Describe the morphology of the red blood cells.
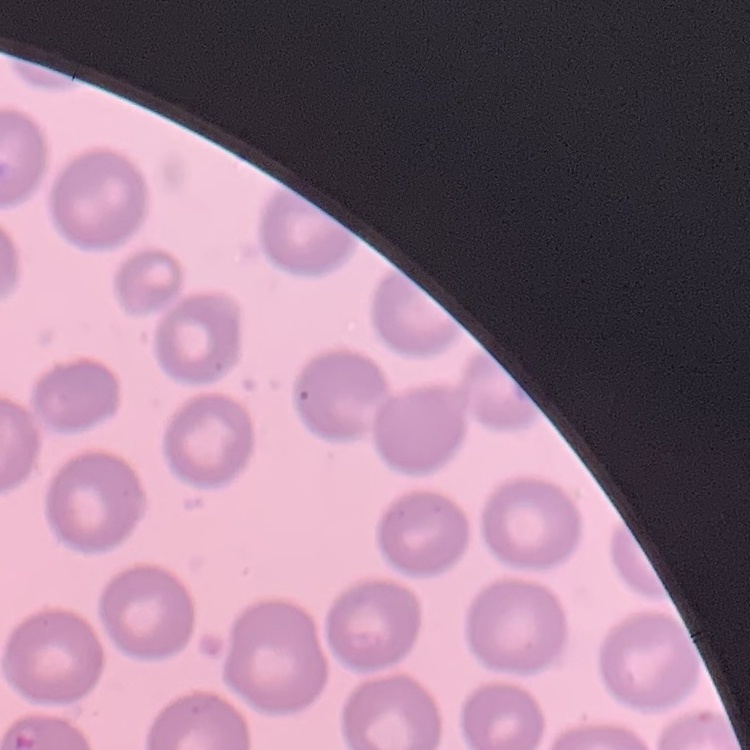
No rouleaux formation.

One tile cut from a larger photomicrograph. Thin blood smear. Field's or Giemsa stain.